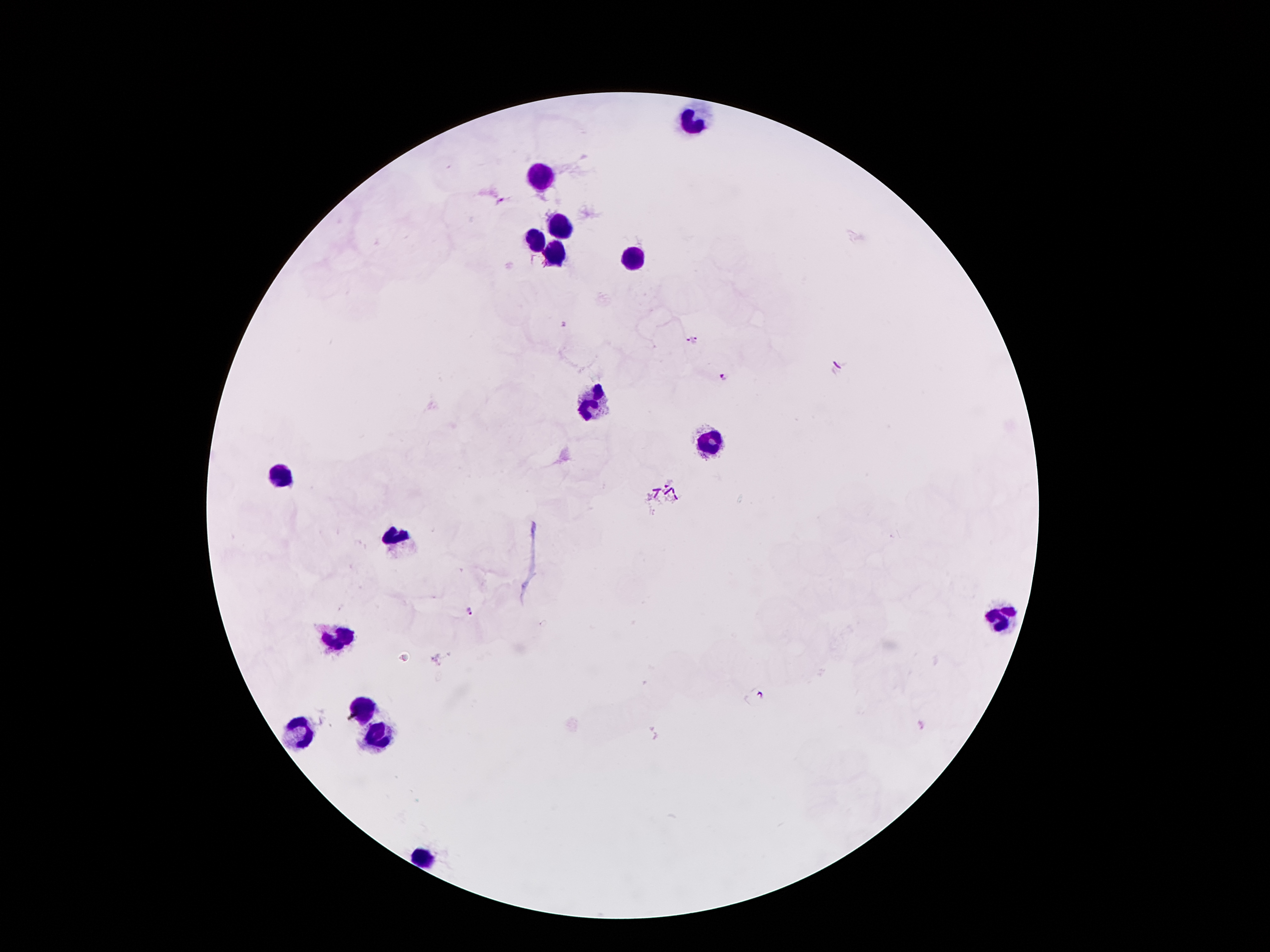

Approximate object centers, in pixels from the top-left corner. Leukocyte locations: (x=693, y=121), (x=535, y=178), (x=558, y=228), (x=535, y=239), (x=550, y=253), (x=632, y=262), (x=594, y=402), (x=707, y=444), (x=283, y=474), (x=403, y=539), (x=1001, y=617), (x=338, y=638), (x=361, y=707), (x=296, y=730), (x=380, y=732), (x=424, y=858). Plasmodium parasite locations: (x=500, y=202), (x=693, y=342), (x=724, y=378), (x=470, y=611). Single field of view. Image is 1270×952 pixels. Thick peripheral-blood smear. Photographed through the microscope eyepiece with a smartphone camera. 100x magnification. Giemsa stain. Patient malaria status: positive for Plasmodium falciparum.